Report the malaria status of this cell.
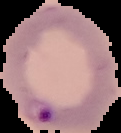

It is parasitized.

Summary:
  - Image size: 121×133 pixels
  - Preparation: thin blood smear
  - Image type: segmented cell region with the area outside set to black